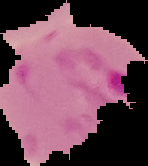
preparation = thin blood smear
image type = segmented cell region with the area outside set to black
image size = 148×166 pixels
malaria status = parasitized